Describe the morphology of the erythrocytes.
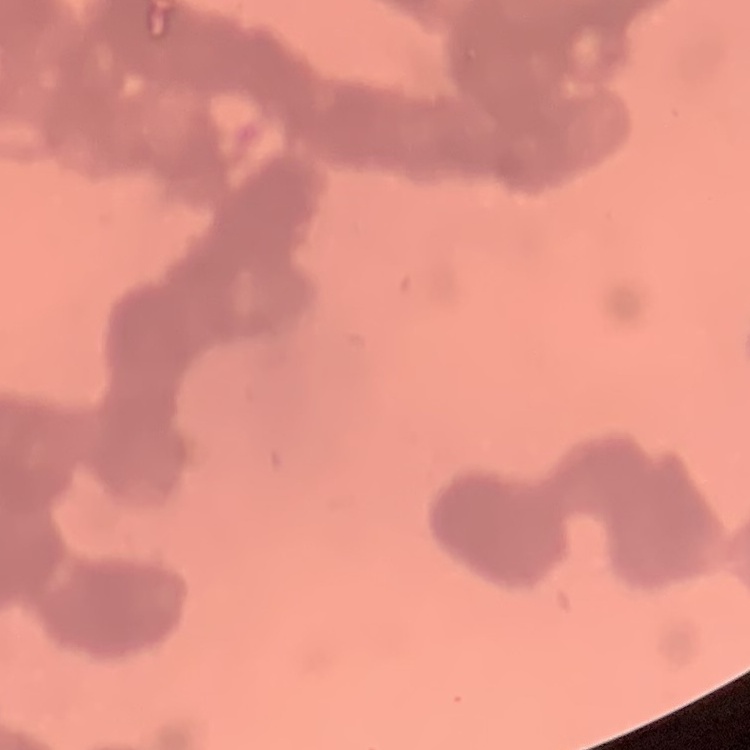

Rouleaux formation.

{
  "image_type": "one tile cut from a larger photomicrograph",
  "preparation": "thin peripheral smear",
  "stain": "Field's or Giemsa"
}